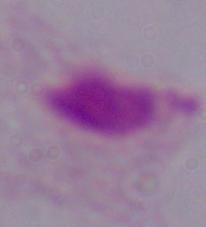
Summary:
  - Magnification: 1000x
  - Modality: photomicrograph
  - Identification: trichomonad